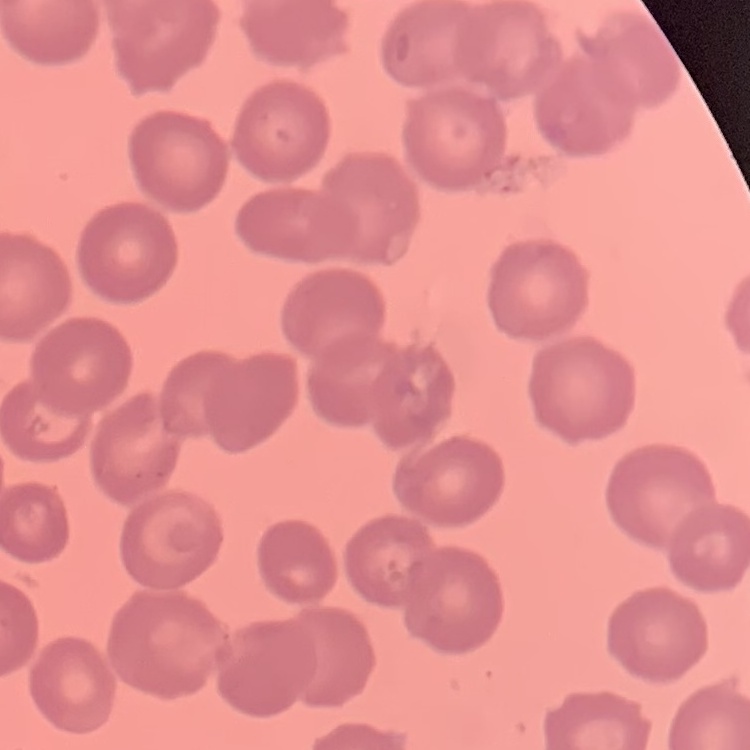
red blood cell morphology = no rouleaux formation
image type = square crop of a larger photomicrograph
preparation = thin blood film
stain = Field's or Giemsa